Report the malaria status of this cell.
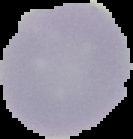
Uninfected.

From a thin blood smear. Image is 133×139 pixels. The area outside the segmented cell region is set to black.